Assess this cell for malaria.
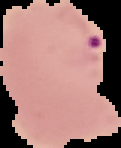
Parasitized.

Image is 121×148 pixels. Cell region segmented out of the field of view; the surrounding area is masked to black. From a thin blood smear.